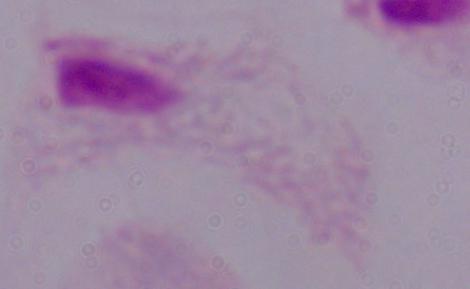

Summary:
  - Modality: photomicrograph
  - Identification: trichomonad
  - Magnification: 1000x